Comment on the morphology of the erythrocytes.
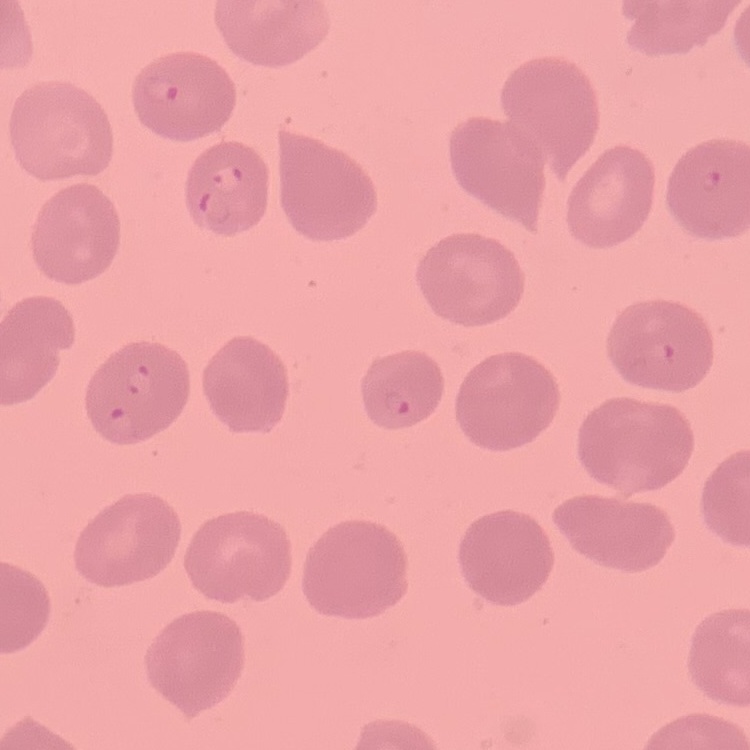

They show no rouleaux formation.

Thin peripheral smear. Stained with either Field's or Giemsa. Square crop of a larger photomicrograph.